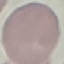
Summary:
  - Malaria status: uninfected
  - Capture: smartphone camera at the microscope eyepiece
  - Image type: automatically extracted cell patch, resized to 64 × 64 pixels
  - Stain: Giemsa
  - Preparation: thin blood film